Outline each blood parasite and name the species.
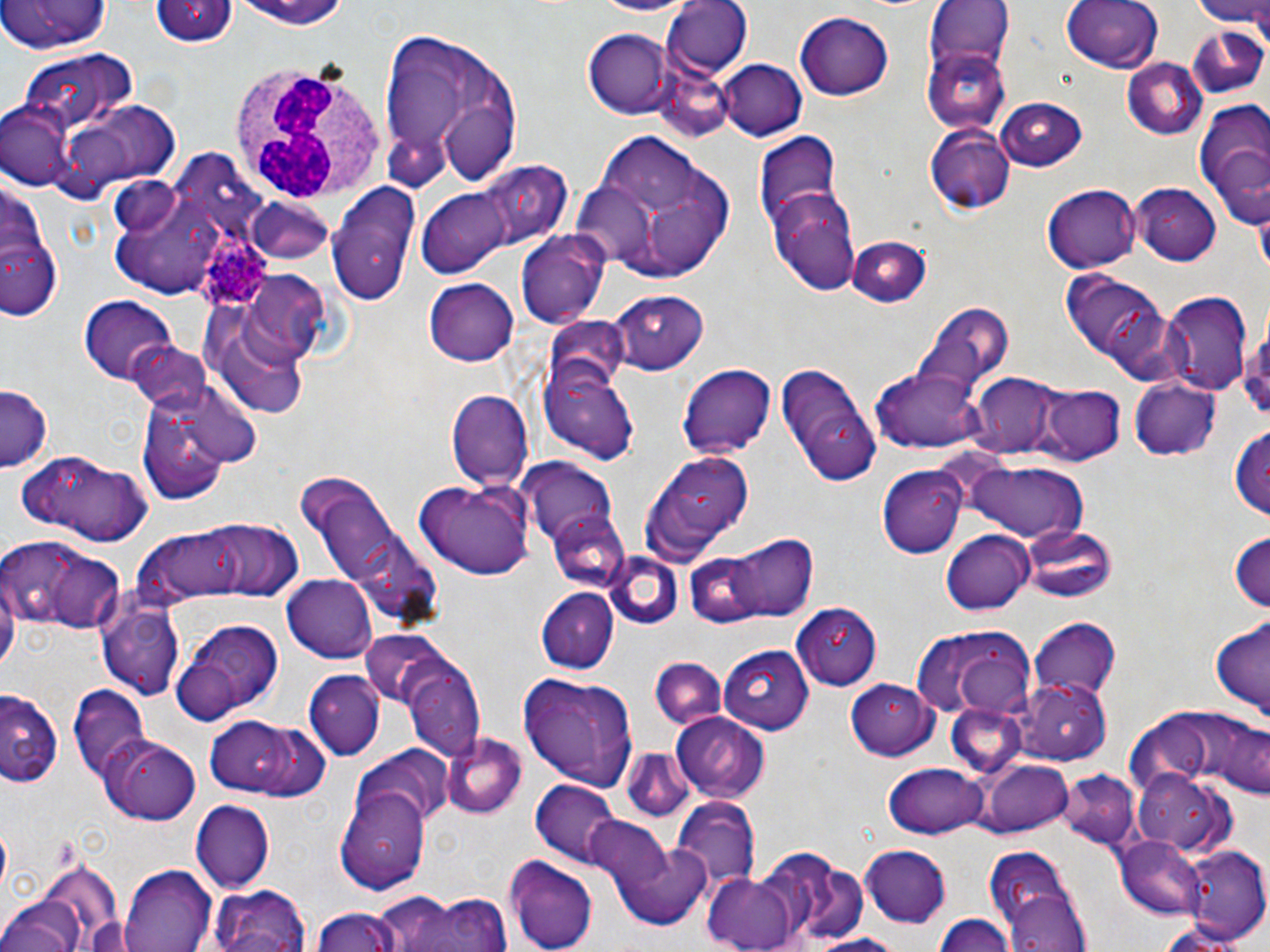

Approximate bounding boxes as [x1, y1, x2, y2] in pixels.
Plasmodium ovale-infected red blood cells: [189, 212, 281, 315].
No Plasmodium falciparum, Plasmodium malariae, Plasmodium vivax, Babesia divergens, or Trypanosoma brucei observed.

White blood cell locations: [227, 62, 389, 207]. Uninfected red blood cell locations: [0, 0, 111, 57], [587, 0, 698, 16], [1060, 0, 1164, 74], [1195, 0, 1270, 36], [152, 1, 236, 48], [225, 1, 358, 33], [923, 1, 1016, 100], [662, 2, 751, 78], [795, 11, 896, 101], [1183, 24, 1269, 99], [583, 29, 674, 118], [377, 30, 523, 190], [923, 42, 1013, 137], [15, 50, 136, 135], [716, 58, 806, 141], [1120, 58, 1208, 142], [650, 70, 734, 143], [59, 97, 183, 197], [994, 98, 1089, 170], [2, 100, 74, 189], [1193, 108, 1270, 228], [928, 125, 1015, 213], [577, 132, 738, 285], [755, 134, 842, 228], [442, 159, 578, 265], [1, 172, 62, 327], [326, 181, 420, 308], [415, 182, 520, 276], [1046, 183, 1142, 271], [1131, 184, 1224, 268], [113, 185, 224, 297], [768, 189, 861, 293], [246, 197, 338, 264], [516, 229, 609, 327], [845, 236, 932, 308], [1063, 273, 1172, 377], [424, 278, 519, 366], [608, 290, 708, 374], [1162, 291, 1253, 395], [199, 293, 317, 419], [79, 295, 180, 382], [910, 304, 1011, 389], [1240, 321, 1270, 428], [123, 340, 214, 415], [540, 340, 642, 466], [774, 361, 881, 489], [676, 362, 776, 461], [869, 365, 991, 453], [967, 373, 1065, 459], [1128, 377, 1221, 462], [0, 385, 52, 471], [1039, 385, 1124, 463], [448, 391, 533, 489], [138, 395, 235, 506], [1230, 424, 1270, 526], [16, 451, 156, 545], [641, 452, 756, 560], [519, 461, 618, 546], [959, 461, 1092, 545], [879, 466, 968, 557], [292, 474, 444, 632], [411, 477, 534, 580], [547, 510, 634, 594], [197, 518, 301, 601], [138, 520, 266, 601], [1021, 524, 1115, 605], [1228, 528, 1270, 615], [941, 529, 1035, 616], [725, 532, 816, 622], [3, 538, 124, 631], [605, 552, 682, 628], [684, 554, 766, 629], [1, 573, 18, 679], [282, 573, 377, 662], [535, 588, 619, 672], [97, 602, 183, 698], [790, 602, 881, 687], [174, 616, 286, 752], [1029, 616, 1121, 700], [1210, 616, 1269, 722], [912, 626, 1039, 720], [361, 633, 454, 713], [719, 645, 818, 733], [396, 653, 484, 761], [648, 659, 729, 731], [304, 671, 388, 761], [518, 671, 641, 791], [846, 677, 939, 760], [1010, 682, 1112, 762], [69, 686, 150, 780], [1, 691, 61, 786], [946, 704, 1030, 779], [1154, 709, 1270, 800], [672, 712, 770, 801], [201, 717, 309, 797], [438, 733, 528, 819], [100, 736, 201, 825], [355, 746, 454, 831], [623, 748, 694, 822], [974, 761, 1073, 836], [885, 764, 987, 837], [1057, 769, 1142, 850], [1136, 769, 1232, 850], [532, 781, 621, 864], [335, 785, 432, 891], [672, 799, 760, 890], [191, 801, 272, 891], [582, 817, 672, 894], [607, 835, 716, 930], [1116, 836, 1207, 920], [859, 844, 953, 927], [983, 844, 1088, 949], [1182, 845, 1270, 947], [766, 850, 869, 942], [503, 854, 597, 952], [31, 864, 124, 946], [119, 866, 214, 952], [702, 870, 808, 952], [211, 882, 312, 952], [398, 889, 516, 952], [1002, 891, 1090, 952], [0, 897, 84, 952], [306, 906, 408, 952], [932, 913, 1017, 951], [799, 933, 909, 952]. Slide-level diagnosis: Plasmodium ovale. Image is 1270×952 pixels. Thin blood film. May-Grünwald-Giemsa stain. One field of a larger specimen. Captured at 1000x magnification. Optical microscopy.